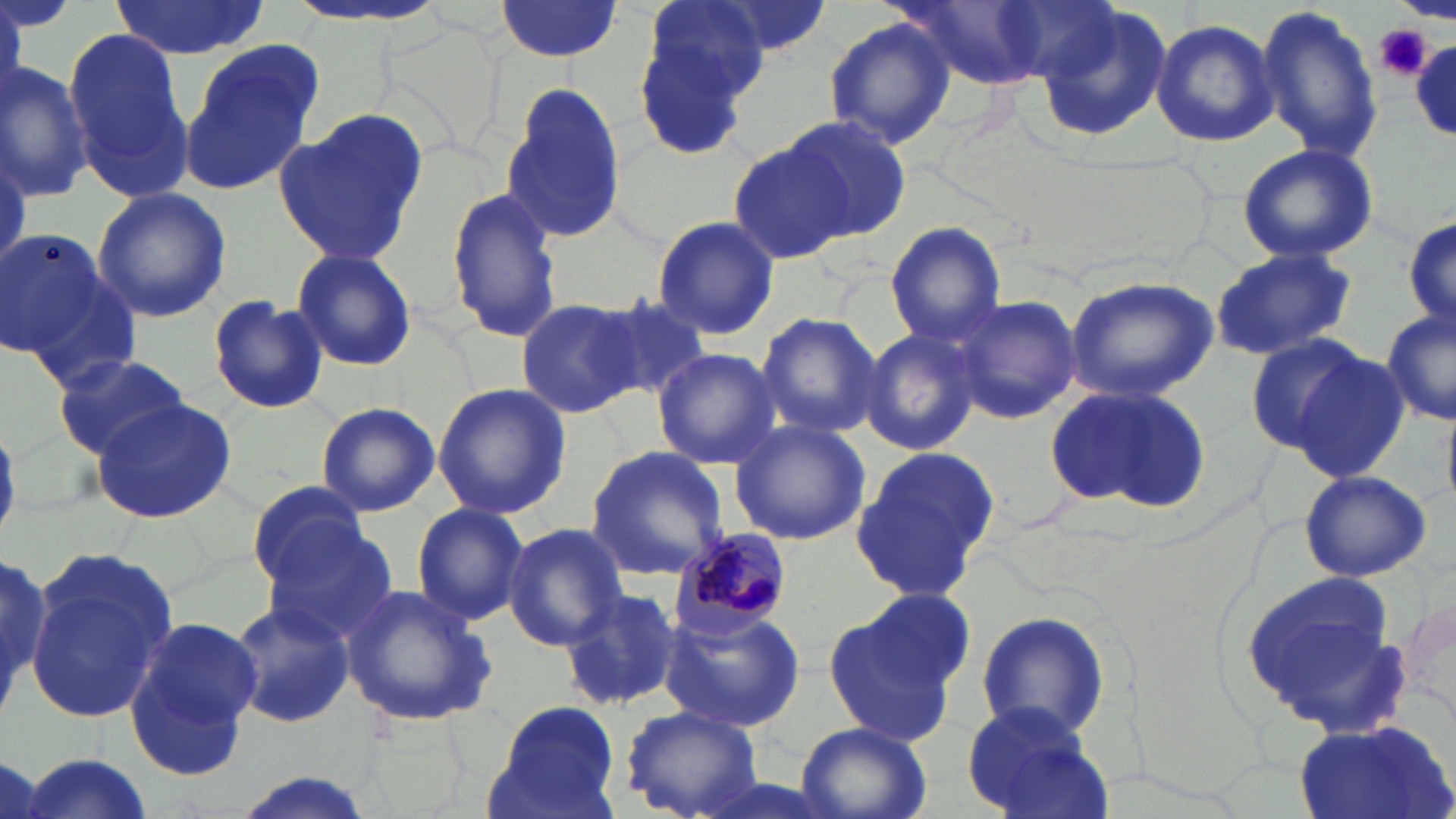

Summary:
  - Coordinate format: approximate bounding boxes as [x1, y1, x2, y2] in pixels
  - Plasmodium malariae-infected red blood cell locations: [667, 528, 796, 638]
  - Platelet locations: [1374, 24, 1431, 81]
  - Uninfected red blood cell locations: [286, 0, 451, 30], [491, 0, 625, 61], [635, 1, 769, 135], [697, 1, 835, 60], [111, 2, 267, 58], [1253, 3, 1383, 164], [1032, 5, 1169, 140], [824, 17, 957, 149], [1151, 19, 1281, 148], [64, 28, 190, 195], [1409, 39, 1456, 135], [178, 41, 324, 194], [1, 59, 94, 203], [501, 85, 628, 244], [273, 111, 430, 263], [783, 116, 912, 243], [726, 136, 856, 266], [1234, 143, 1380, 263], [445, 184, 563, 345], [91, 187, 232, 324], [1402, 211, 1456, 338], [650, 215, 778, 342], [883, 221, 1006, 347], [2, 229, 119, 370], [1209, 249, 1356, 362], [289, 250, 418, 375], [20, 271, 143, 394], [1063, 274, 1219, 402], [591, 291, 712, 404], [950, 294, 1081, 425], [206, 295, 328, 415], [515, 297, 643, 419], [1381, 308, 1455, 424], [756, 310, 883, 438], [861, 326, 984, 456], [1242, 332, 1375, 453], [1281, 347, 1411, 480], [652, 349, 779, 468], [53, 353, 190, 458], [1042, 382, 1213, 514], [432, 383, 571, 520], [90, 397, 237, 525], [314, 401, 441, 516], [727, 417, 870, 546], [850, 444, 1002, 602], [587, 447, 729, 578], [1298, 469, 1433, 580], [246, 478, 372, 594], [410, 502, 530, 626], [258, 518, 402, 648], [502, 524, 628, 649], [0, 549, 64, 712], [23, 553, 179, 728], [1234, 570, 1410, 732], [558, 584, 684, 712], [340, 585, 497, 728], [821, 595, 972, 750], [1400, 596, 1456, 728], [224, 599, 355, 728], [658, 606, 806, 733], [976, 611, 1111, 744], [124, 617, 262, 780], [483, 700, 622, 819], [963, 700, 1114, 819], [621, 704, 763, 819], [1294, 714, 1456, 819], [795, 721, 932, 819], [14, 752, 154, 818], [225, 774, 381, 819]
  - Slide-level diagnosis: Plasmodium malariae
  - Field of view: single
  - Preparation: thin blood film
  - Stain: May-Grünwald-Giemsa
  - Magnification: 1000x
  - Modality: optical microscopy
  - Image size: 1456×819 pixels